Assess this cell for malaria.
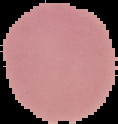
It is uninfected.

preparation = thin blood film
image type = segmented cell region with the area outside set to black
image size = 118×124 pixels